Describe the morphology of the erythrocytes.
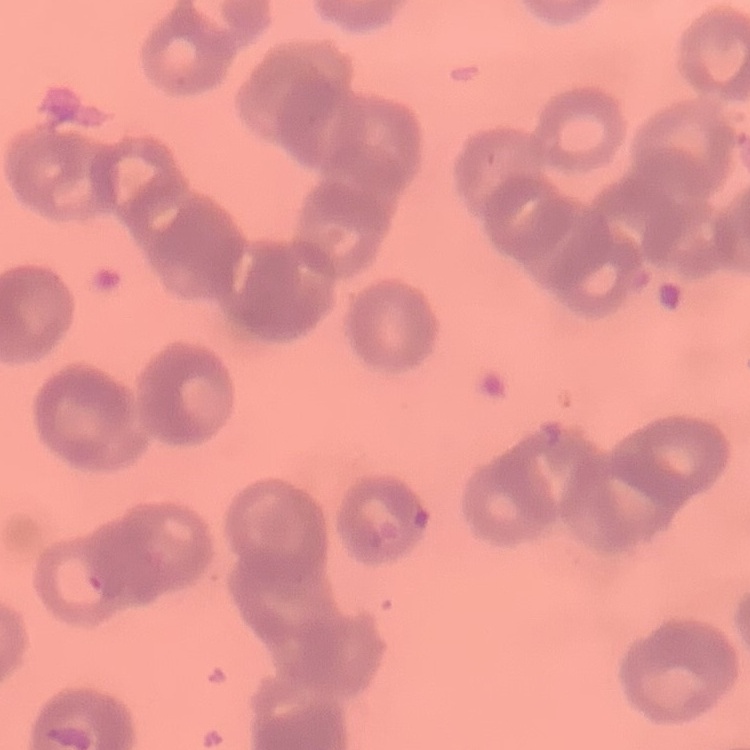
Rouleaux formation.

Thin blood film. Square crop of a larger photomicrograph. Field's or Giemsa stain.